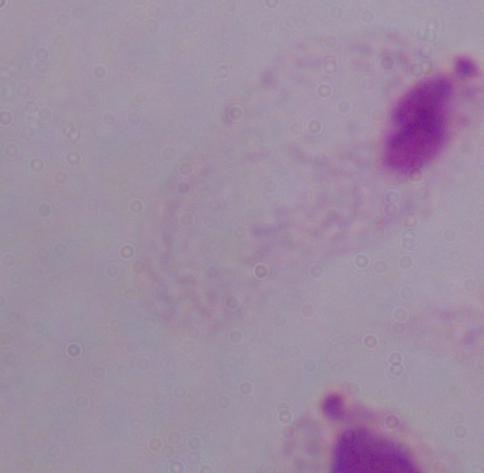

{
  "magnification": "1000x",
  "identification": "trichomonad",
  "modality": "micrograph"
}